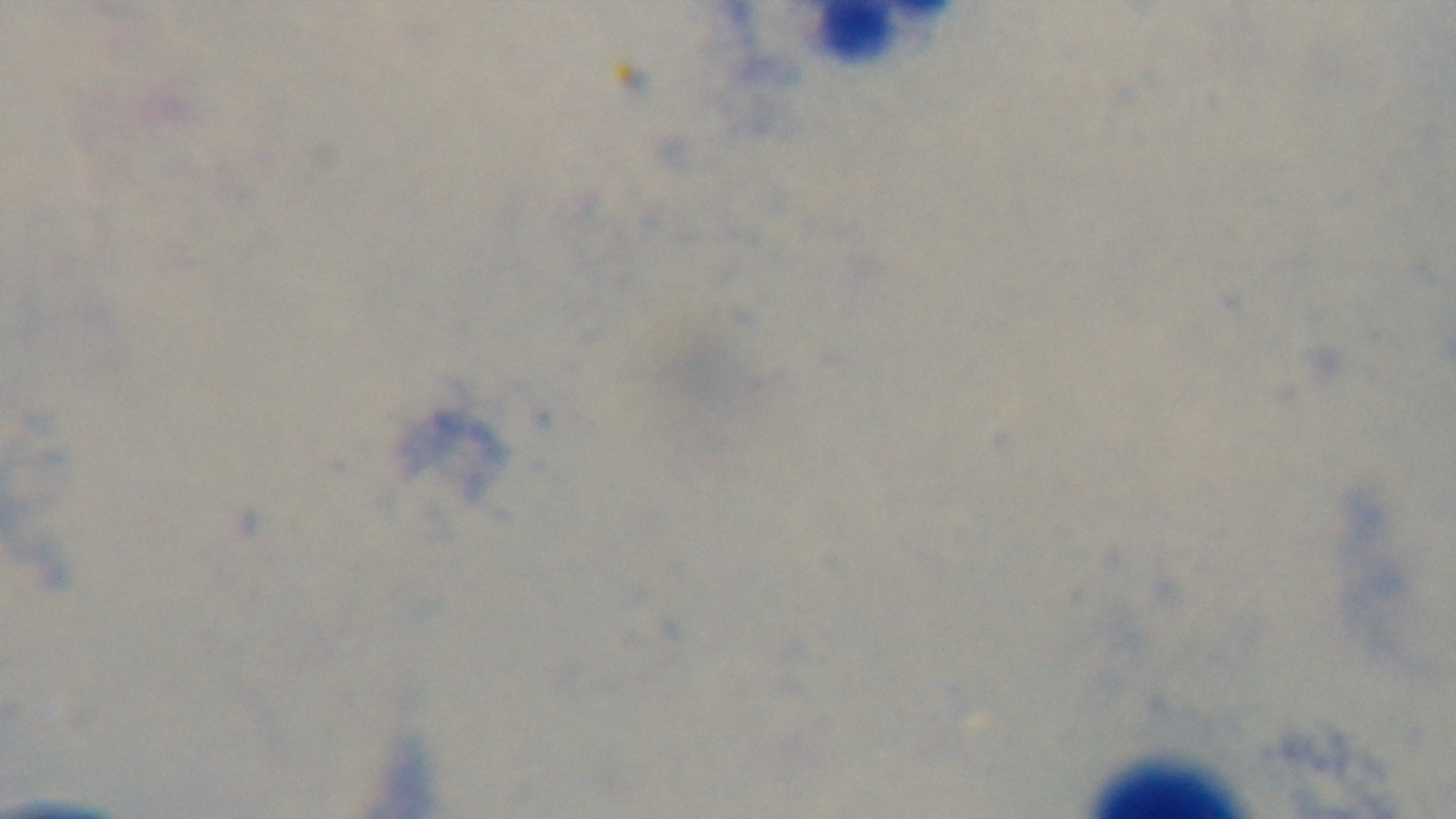
field of view = one from the slide
stain = Giemsa
preparation = thick smear
malaria status = negative
objective = 100x oil immersion
modality = light microscopy
capture = mounted 4K digital camera